Draw a bounding box around every leukocyte (white blood cell).
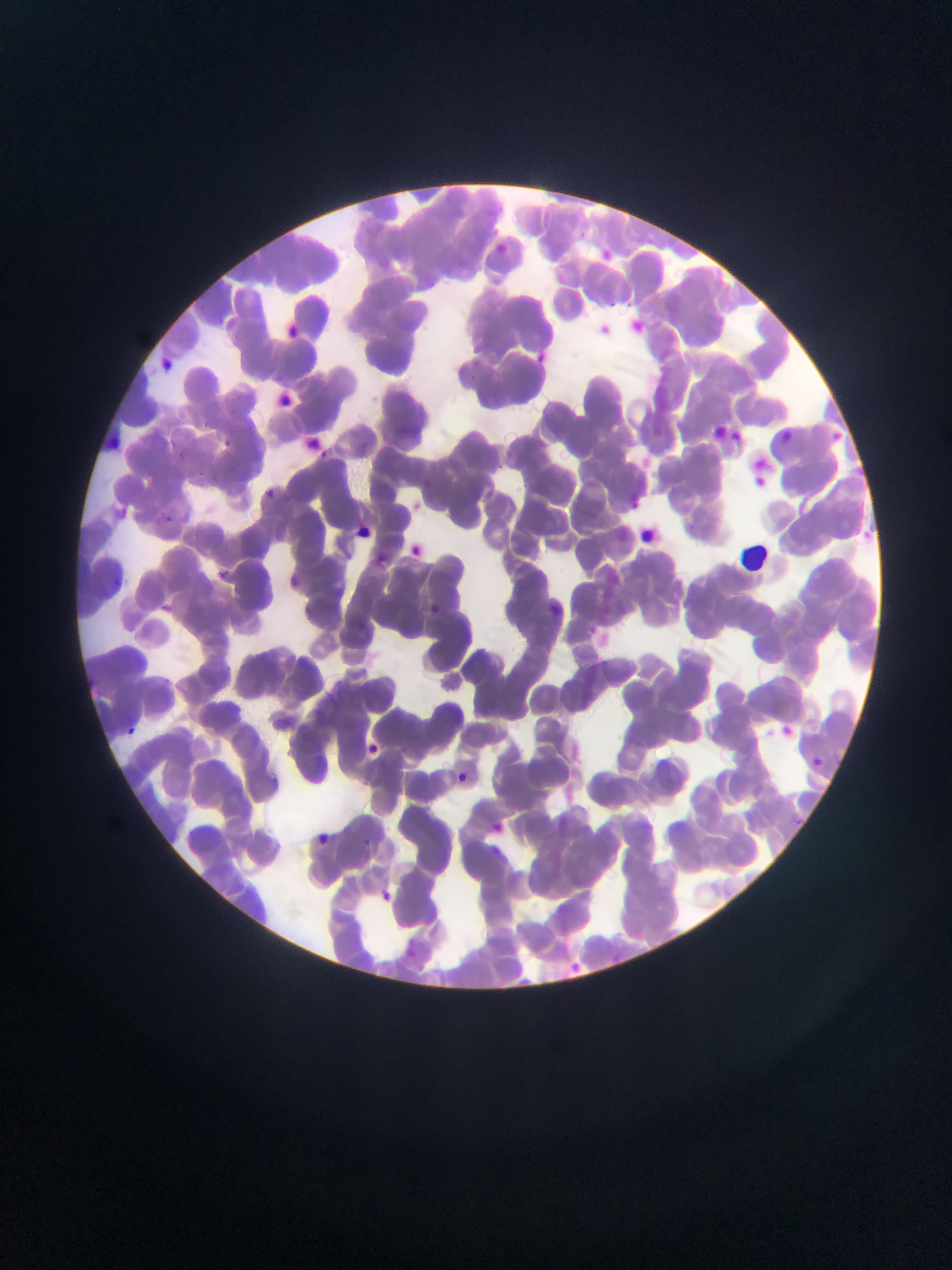

No leukocytes observed.

Approximate bounding boxes as (left, top, right, bottom) in pixels.
Summary:
  - Malaria parasite locations: (496, 239, 510, 253), (601, 247, 623, 260), (273, 319, 318, 341), (539, 346, 553, 364), (278, 390, 300, 413), (713, 419, 731, 438), (400, 421, 422, 436), (729, 425, 746, 444), (830, 425, 841, 440), (783, 427, 805, 448), (219, 436, 234, 451), (314, 445, 331, 461), (755, 476, 769, 493), (262, 487, 277, 502), (157, 511, 176, 528), (855, 526, 878, 546), (411, 540, 427, 558), (214, 568, 229, 582), (282, 573, 313, 591), (159, 597, 182, 619), (422, 603, 443, 618), (779, 721, 795, 746), (122, 724, 140, 740), (365, 743, 383, 758), (809, 755, 825, 771), (449, 767, 472, 788), (310, 831, 333, 850), (373, 887, 396, 906), (404, 945, 420, 965)
  - Preparation: thin blood smear
  - Country: Ghana
  - Field of view: single
  - Capture: mobile-phone photograph through a microscope
  - Image size: 952×1270 pixels